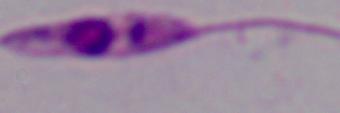

modality = photomicrograph
identification = Leishmania
magnification = 1000x